Locate every Plasmodium parasite.
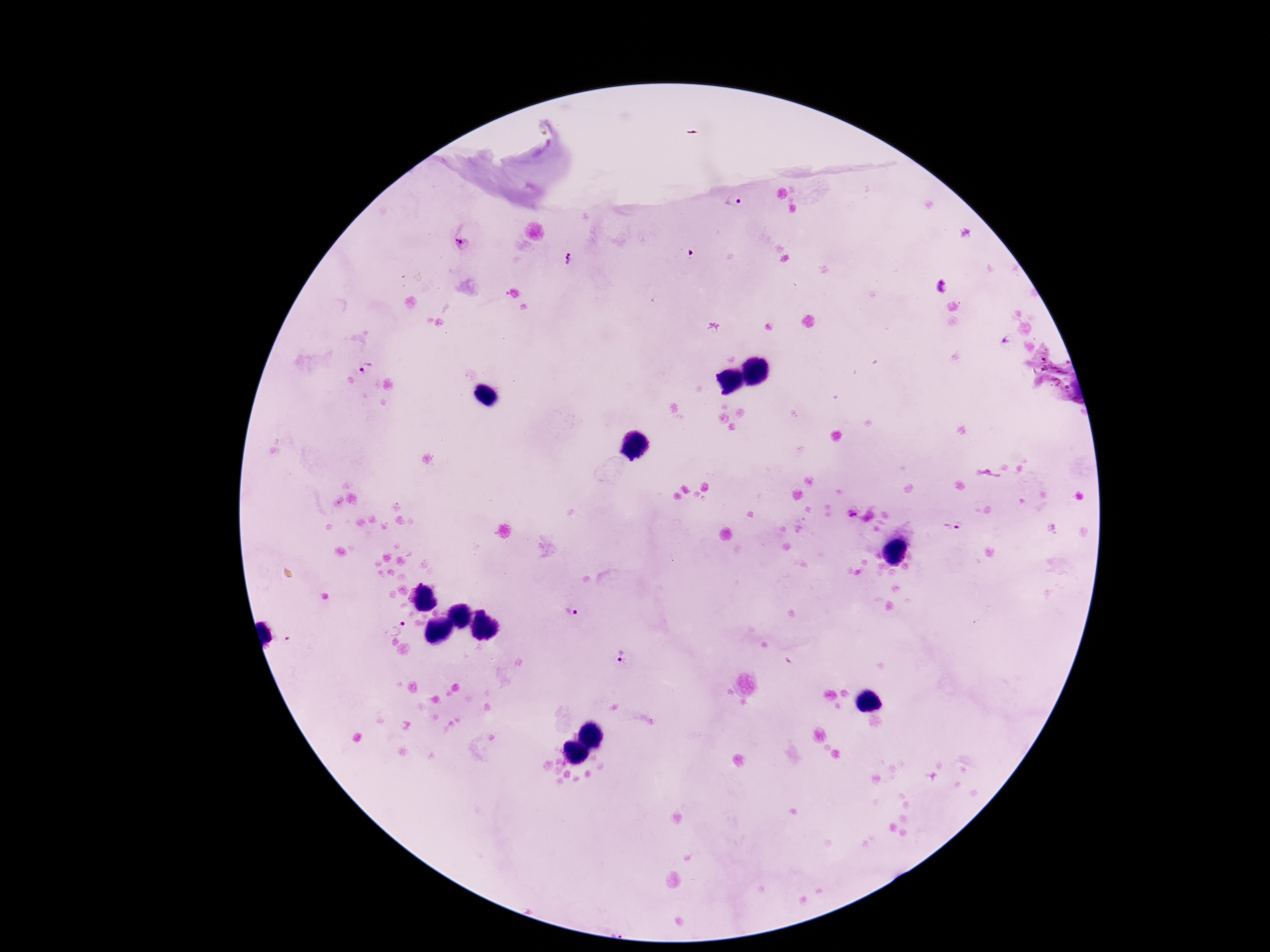
Approximate object centers, in pixels from the top-left corner.
Plasmodium parasites: (x=734, y=203), (x=461, y=242), (x=569, y=260), (x=942, y=287), (x=365, y=368), (x=852, y=514), (x=954, y=528), (x=570, y=613), (x=392, y=624), (x=622, y=655).

Patient malaria status: infected. Image is 1270×952 pixels. Giemsa-stained preparation. 100x magnification. Thick blood film. Smartphone photograph taken through the microscope eyepiece. Single field of view.